Point out each leukocyte.
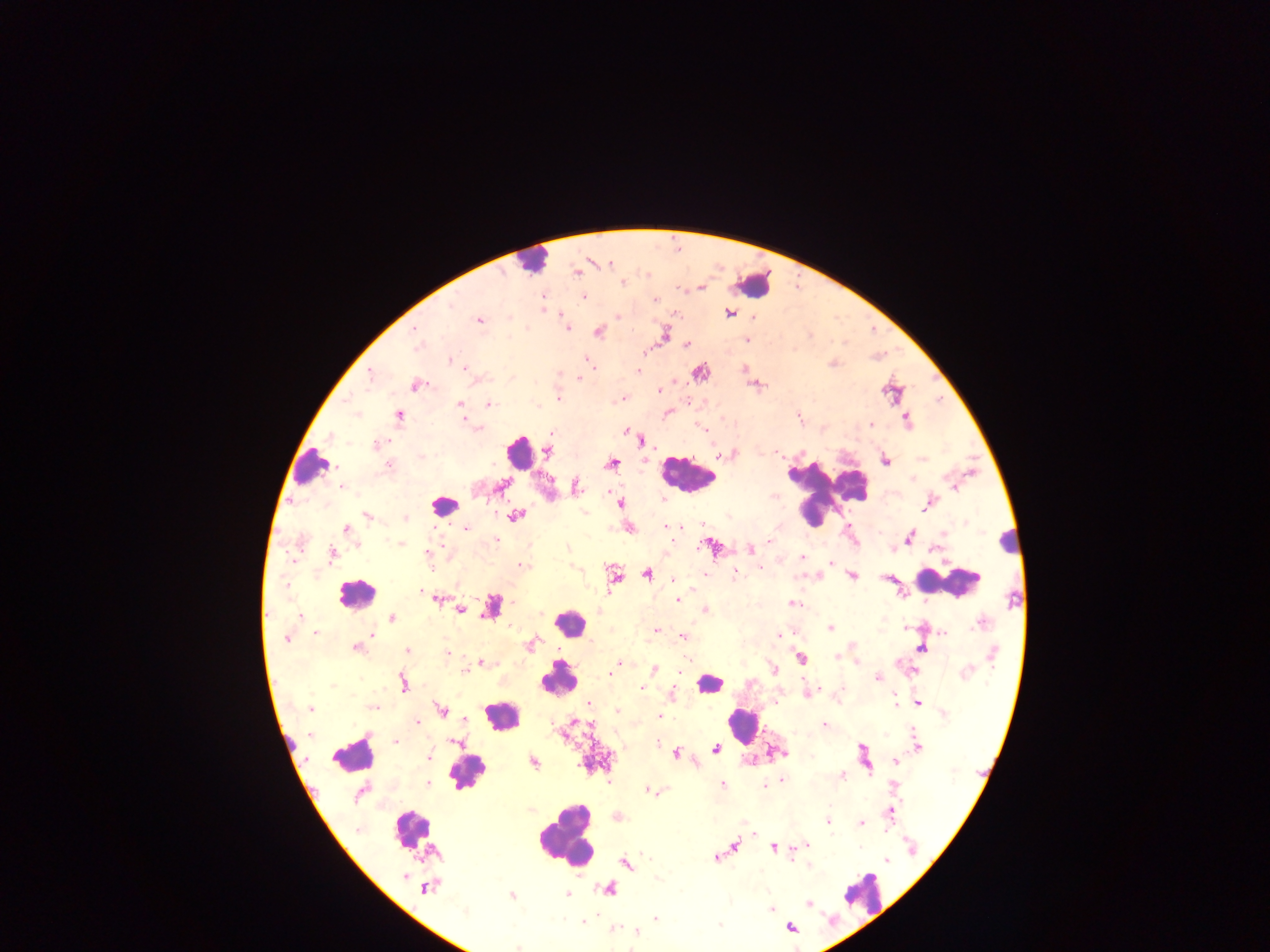

Approximate centers as [x, y] in pixels.
Leukocytes: [529, 261], [753, 283], [518, 452], [312, 467], [687, 474], [825, 492], [442, 507], [1010, 538], [950, 582], [356, 594], [569, 623], [558, 679], [709, 683], [502, 715], [742, 725], [351, 755], [464, 766], [412, 829], [566, 835], [862, 893].

Malaria parasite locations: [610, 263], [576, 272], [623, 284], [583, 297], [655, 299], [452, 305], [729, 313], [618, 317], [509, 318], [480, 320], [567, 328], [415, 330], [599, 332], [665, 334], [747, 340], [687, 344], [417, 347], [586, 360], [451, 361], [462, 367], [638, 372], [371, 375], [579, 378], [418, 384], [659, 390], [558, 398], [459, 404], [489, 404], [356, 415], [399, 415], [907, 419], [870, 425], [477, 429], [626, 430], [703, 430], [331, 437], [376, 444], [549, 451], [420, 457], [612, 462], [886, 462], [388, 464], [503, 485], [576, 486], [341, 487], [664, 499], [621, 504], [927, 505], [584, 513], [367, 516], [515, 516], [729, 516], [405, 518], [673, 527], [678, 527], [667, 528], [346, 529], [466, 529], [943, 533], [909, 537], [402, 538], [497, 540], [769, 541], [400, 543], [708, 544], [567, 549], [750, 550], [428, 553], [332, 555], [802, 557], [831, 563], [521, 565], [760, 568], [704, 573], [647, 574], [735, 575], [853, 576], [614, 577], [674, 580], [286, 584], [420, 591], [439, 599], [678, 601], [792, 603], [704, 609], [461, 610], [300, 615], [392, 618], [980, 623], [830, 627], [655, 631], [943, 633], [315, 634], [372, 635], [779, 635], [683, 637], [286, 639], [922, 648], [357, 649], [408, 650], [447, 653], [993, 654], [836, 657], [801, 658], [857, 662], [482, 663], [619, 663], [655, 668], [774, 669], [614, 670], [681, 671], [465, 672], [610, 673], [966, 673], [877, 678], [403, 683], [333, 685], [641, 688], [808, 693], [672, 694], [894, 701], [775, 703], [918, 703], [589, 704], [374, 707], [310, 708], [441, 709], [617, 710], [944, 713], [661, 716], [465, 719], [418, 723], [824, 724], [397, 741], [455, 742], [657, 744], [918, 746], [716, 749], [676, 754], [429, 758], [896, 761], [534, 763], [843, 775], [782, 780], [609, 781], [427, 784], [722, 784], [763, 786], [894, 786], [647, 791], [891, 814], [828, 822], [861, 823], [753, 834], [735, 845], [806, 845], [773, 847], [911, 847], [716, 857], [886, 860], [625, 862], [809, 866], [405, 876], [657, 879], [425, 888], [609, 889], [511, 895], [566, 895], [808, 904], [771, 909], [464, 912], [656, 918], [583, 922], [719, 925], [614, 928], [791, 929], [637, 931], [518, 947]. Single field of view. Sample from Ghana. Image is 1270×952 pixels. Thick blood film. Photographed through a microscope with a mobile-phone camera.